Name the cell type shown.
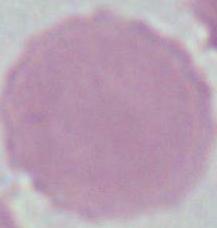
An erythrocyte.

{
  "magnification": "1000x",
  "modality": "micrograph"
}